Comment on the morphology of the red blood cells.
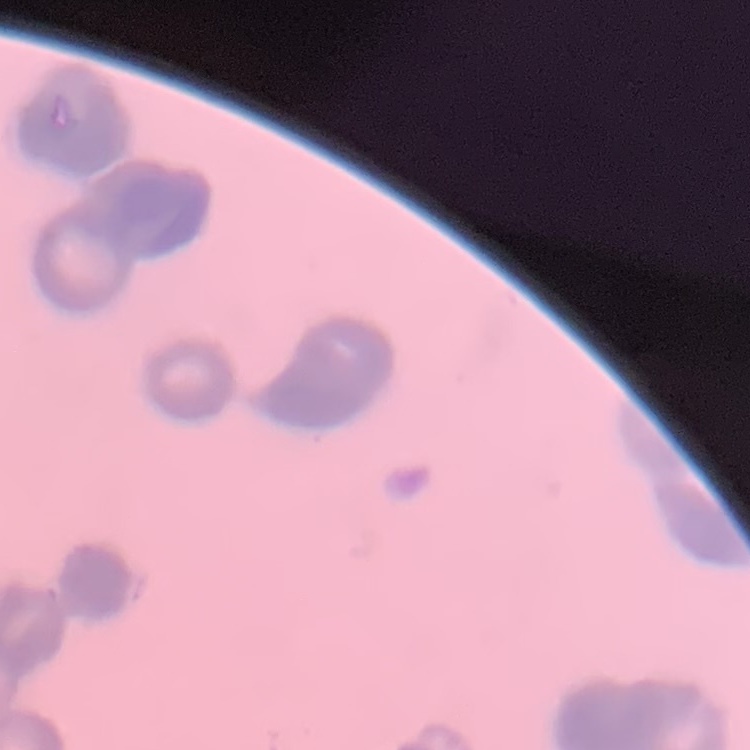

They show rouleaux formation.

Stained with either Field's or Giemsa. Thin blood film. Square crop of a larger photomicrograph.